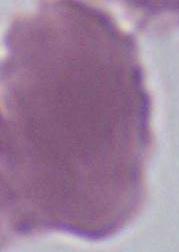 Micrograph. Captured at 1000x magnification. A red blood cell is shown.